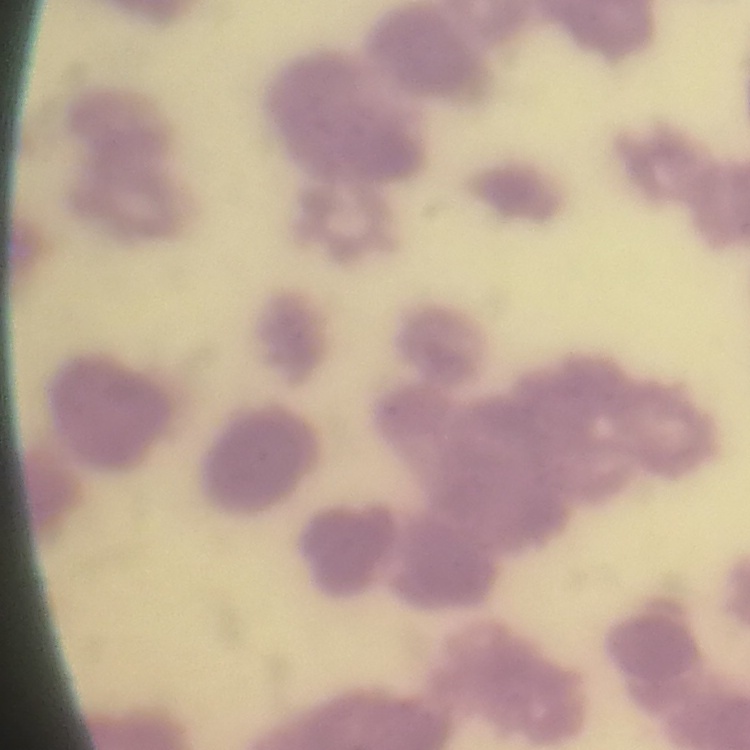

The red blood cells exhibit rouleaux formation. Square crop of a larger photomicrograph. Thin blood smear. Stained with either Field's or Giemsa.